Outline each blood parasite and name the species.
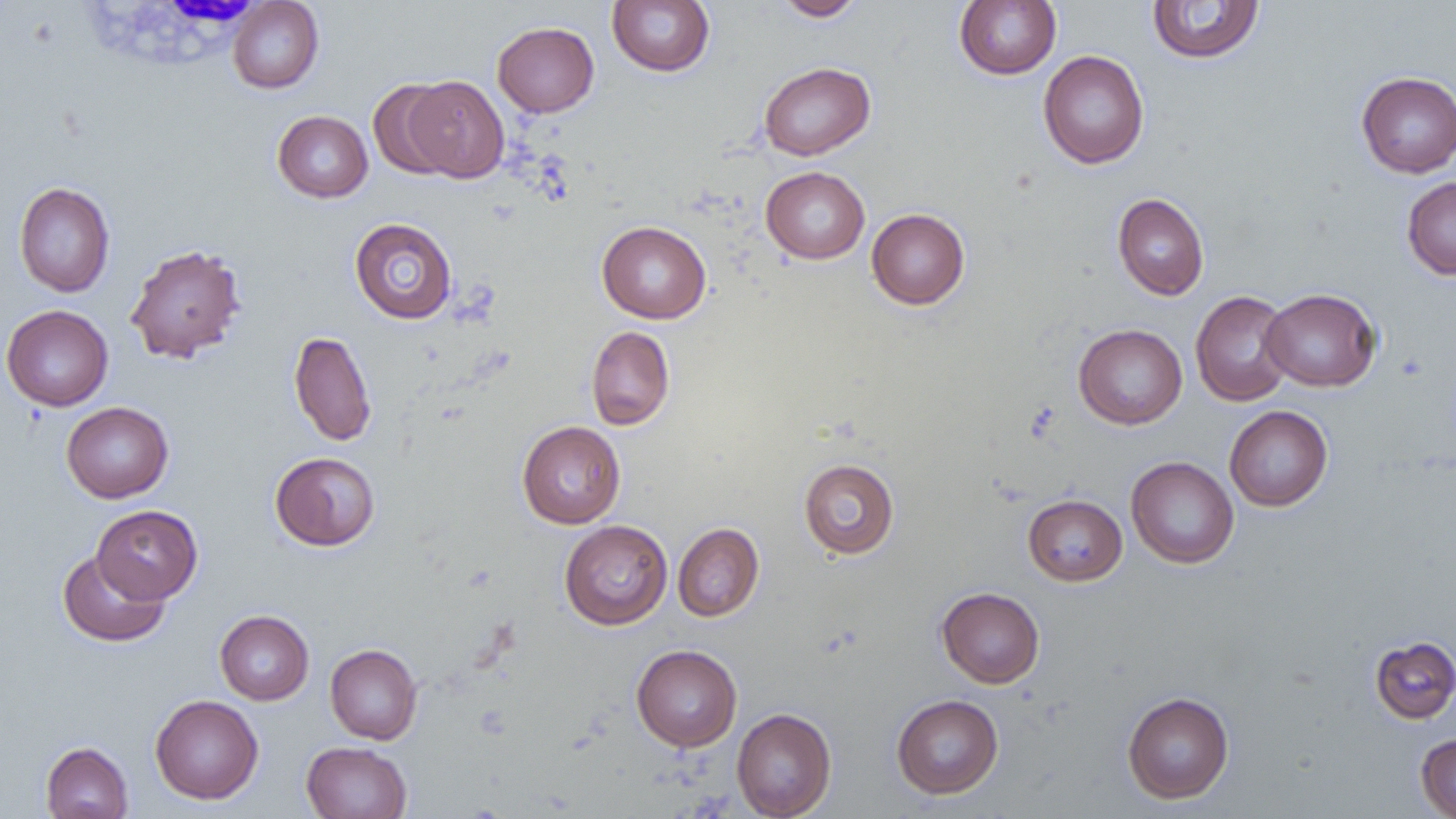
No blood parasites seen.

Approximate bounding boxes as (x1, y1, x2, y2) in pixels. White blood cell locations: (79, 0, 269, 85). Uninfected red blood cell locations: (606, 0, 715, 76), (775, 0, 866, 21), (954, 0, 1062, 80), (227, 1, 324, 93), (1146, 1, 1266, 64), (492, 21, 599, 117), (1038, 50, 1149, 169), (759, 61, 875, 160), (1356, 71, 1456, 177), (404, 75, 510, 183), (367, 80, 459, 180), (272, 110, 373, 203), (760, 166, 870, 264), (1402, 176, 1456, 280), (14, 181, 115, 297), (1112, 193, 1209, 300), (866, 208, 969, 309), (349, 217, 457, 324), (596, 221, 711, 324), (125, 243, 247, 364), (1261, 288, 1381, 392), (1190, 290, 1296, 406), (1, 304, 114, 411), (1073, 324, 1187, 429), (586, 325, 675, 430), (289, 330, 376, 447), (61, 402, 174, 503), (1224, 405, 1333, 511), (517, 421, 626, 528), (270, 451, 380, 551), (1126, 456, 1239, 569), (798, 458, 899, 559), (1023, 494, 1127, 586), (91, 505, 202, 604), (559, 519, 673, 630), (673, 522, 764, 622), (57, 549, 170, 647), (936, 587, 1045, 688), (214, 610, 314, 705), (1369, 635, 1456, 723), (325, 643, 422, 744), (631, 644, 742, 751), (1122, 691, 1234, 804), (150, 694, 264, 804), (891, 694, 1003, 799), (732, 707, 837, 818), (1415, 733, 1456, 818), (40, 741, 133, 819), (301, 741, 412, 819). Slide-level diagnosis: no evidence of blood parasites. One field of a larger specimen. Optical microscopy. 1000x magnification. Image is 1456×819 pixels. Thin blood smear.